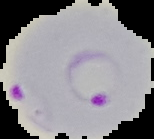

Summary:
  - Malaria status: parasitized
  - Image type: segmented cell region with the area outside set to black
  - Image size: 154×139 pixels
  - Preparation: thin blood film